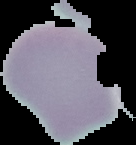

Image is 136×145 pixels. Malaria status: uninfected. Segmented cell region on a black background. From a thin blood smear.